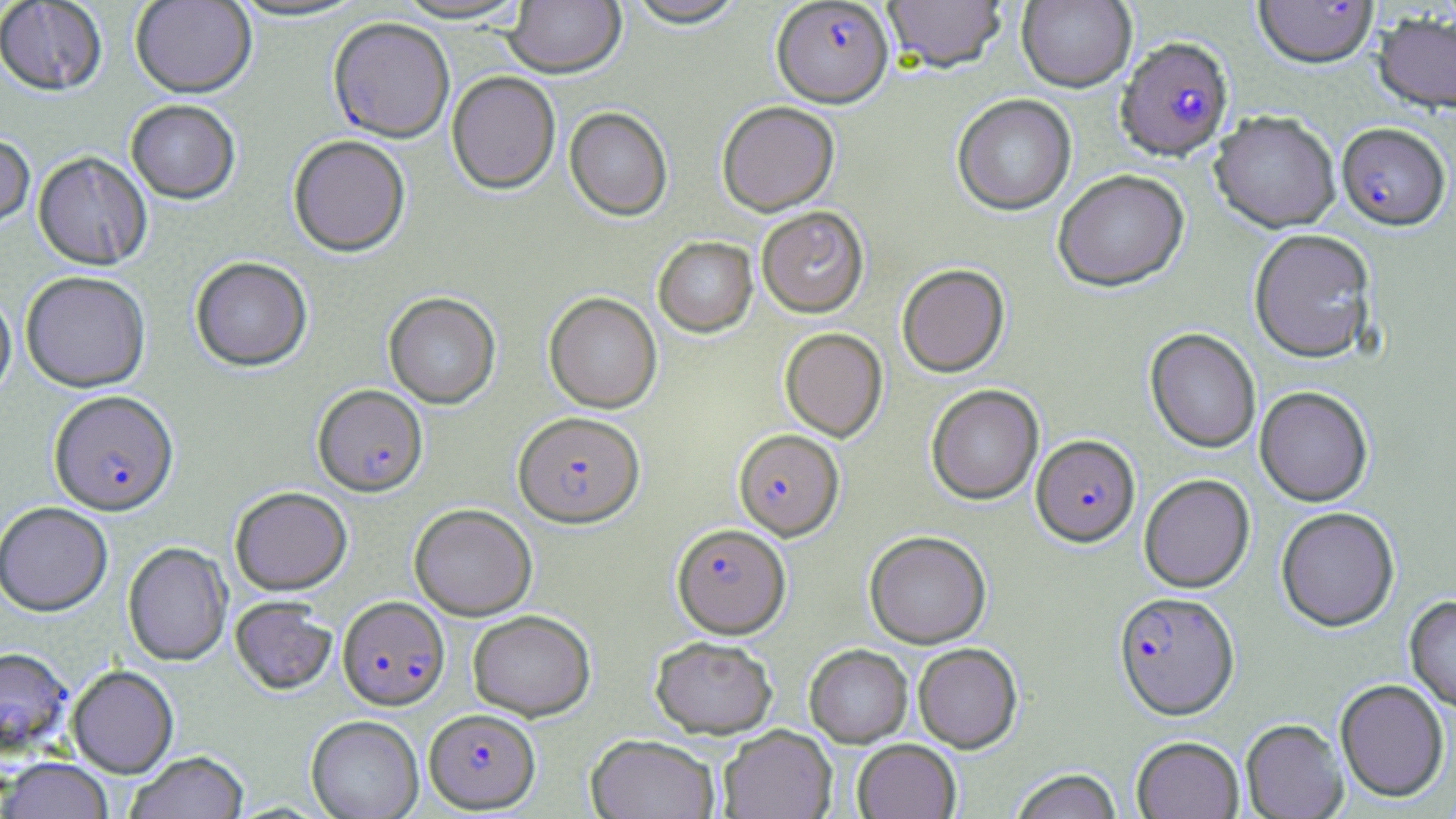

slide_level_diagnosis: Plasmodium falciparum
uninfected_red_blood_cell_locations: 'approximate bounding boxes as (x1, y1, x2, y2) in pixels: (131, 0, 256, 100), (226, 0, 370, 24), (391, 0, 532, 26), (504, 0, 625, 81), (624, 0, 749, 32), (883, 0, 1007, 75), (1017, 0, 1137, 93), (0, 1, 107, 98), (1373, 12, 1456, 116), (446, 74, 560, 196), (952, 95, 1077, 217), (126, 101, 241, 205), (717, 103, 840, 217), (564, 108, 673, 222), (1210, 113, 1340, 233), (0, 136, 35, 233), (288, 137, 410, 259), (33, 153, 152, 270), (1052, 170, 1190, 293), (757, 207, 869, 318), (1249, 229, 1377, 363), (653, 237, 758, 339), (190, 258, 313, 372), (897, 265, 1010, 378), (20, 272, 151, 393), (384, 293, 501, 409), (544, 293, 662, 413), (0, 294, 16, 404), (780, 328, 888, 441), (1145, 328, 1261, 453), (926, 385, 1044, 505), (1254, 386, 1373, 507), (1139, 474, 1255, 593), (230, 487, 352, 596), (0, 502, 113, 616), (409, 504, 537, 621), (1276, 507, 1400, 632), (864, 531, 991, 648), (123, 542, 232, 667), (1405, 595, 1456, 713), (230, 597, 337, 696), (468, 610, 596, 721), (650, 636, 777, 738), (913, 643, 1023, 753), (804, 645, 913, 747), (0, 647, 72, 758), (67, 666, 179, 778), (1335, 679, 1449, 804), (306, 715, 424, 819), (1241, 718, 1348, 819), (717, 725, 837, 819), (586, 734, 721, 819), (1132, 736, 1244, 819), (852, 739, 961, 819), (126, 751, 249, 819), (1, 758, 114, 819), (1009, 769, 1123, 819)'
magnification: 1000x
preparation: thin blood film
plasmodium_falciparum_infected_red_blood_cell_locations: 'approximate bounding boxes as (x1, y1, x2, y2) in pixels: (771, 1, 894, 110), (1253, 1, 1379, 72), (328, 19, 455, 145), (1116, 38, 1234, 164), (1336, 123, 1451, 232), (313, 385, 428, 498), (49, 391, 179, 517), (513, 412, 645, 528), (733, 430, 844, 540), (1031, 435, 1140, 548), (672, 523, 790, 638), (1114, 591, 1239, 720), (338, 596, 450, 710), (424, 708, 541, 813)'
field_of_view: single
image_size: 1456×819 pixels
stain: May-Grünwald-Giemsa
modality: optical microscopy